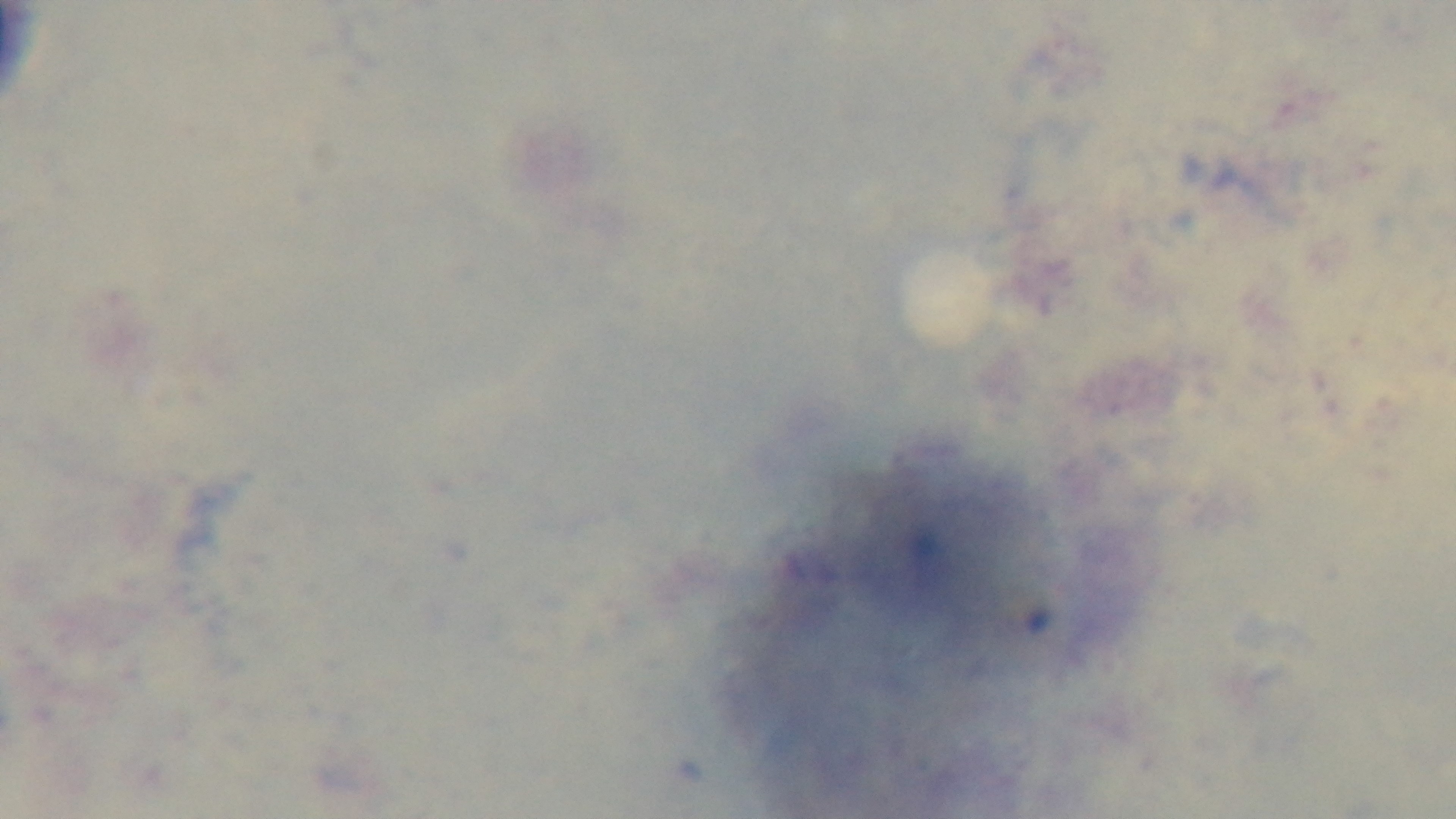

Giemsa-stained. Light microscopy. 100x oil-immersion objective. Captured with a mounted 4K digital camera. Malaria status: negative. Preparation: thick blood film. One field from the slide.